Classify this cell by malaria status.
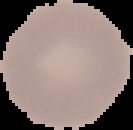
It is uninfected.

Summary:
  - Image size: 133×130 pixels
  - Image type: cell region segmented out of the field of view; surrounding area masked to black
  - Preparation: thin blood film